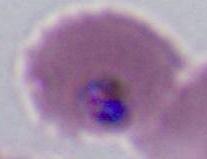
Summary:
  - Modality: photomicrograph
  - Magnification: 400x or 1000x
  - Identification: Plasmodium